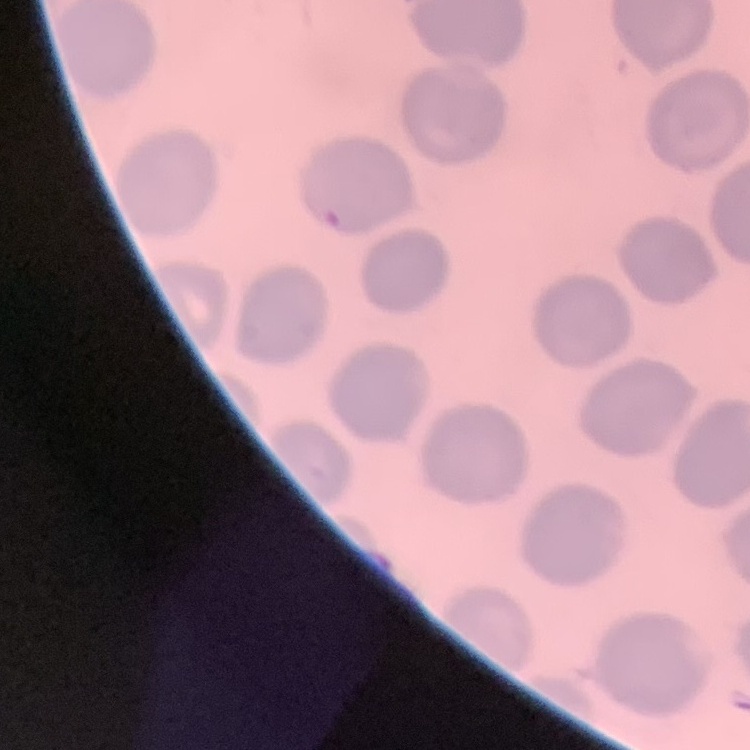
The red blood cells exhibit no rouleaux formation. Square crop of a larger photomicrograph. Field's or Giemsa stain. Thin blood smear.